Assess the morphology of the erythrocytes.
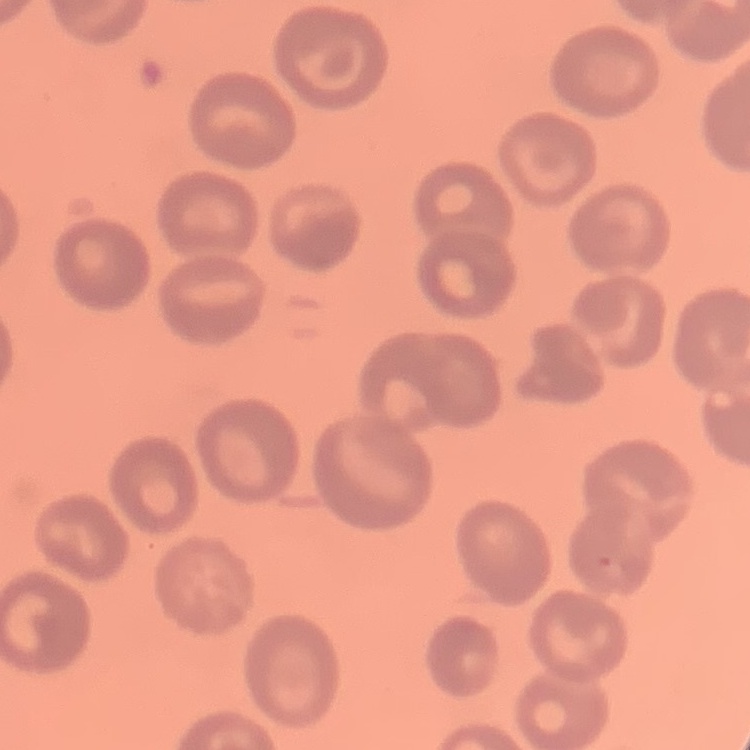

They show no rouleaux formation.

Thin blood film. Field's or Giemsa stain. Square crop of a larger photomicrograph.